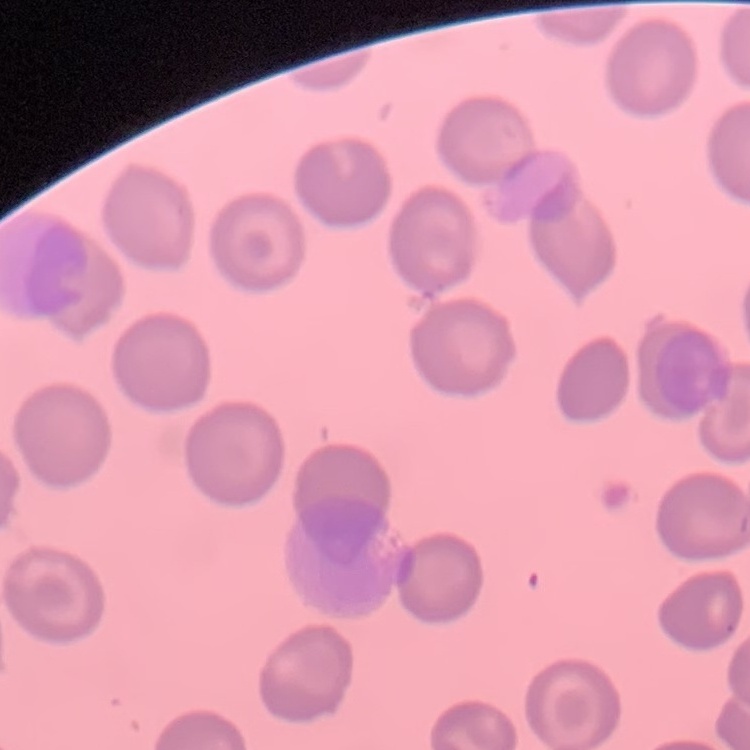

The erythrocytes show no rouleaux formation. Thin blood film. Square crop of a larger photomicrograph. Stained with either Field's or Giemsa.